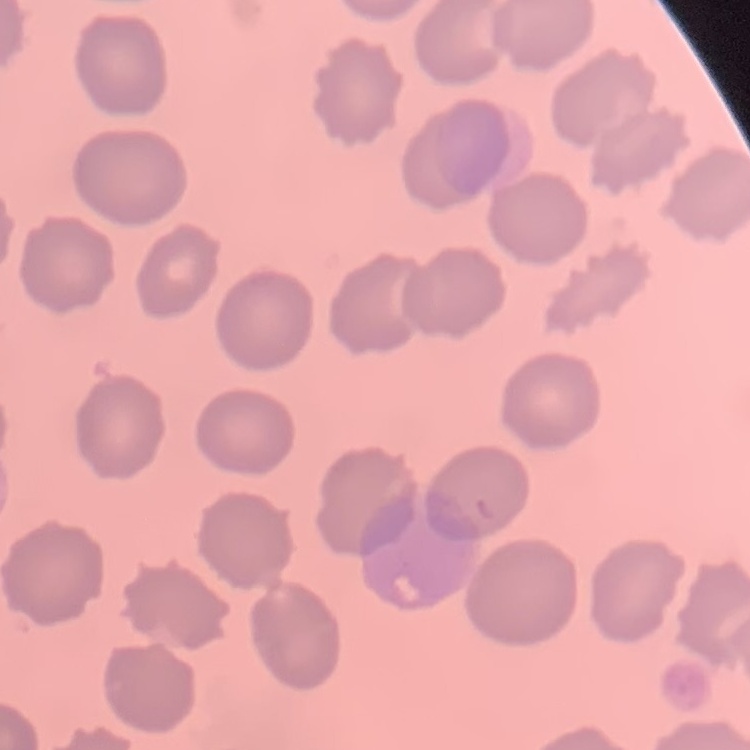
red blood cell morphology = no rouleaux formation
stain = Field's or Giemsa
image type = square crop of a larger photomicrograph
preparation = thin peripheral smear